Locate every malaria parasite and every leukocyte.
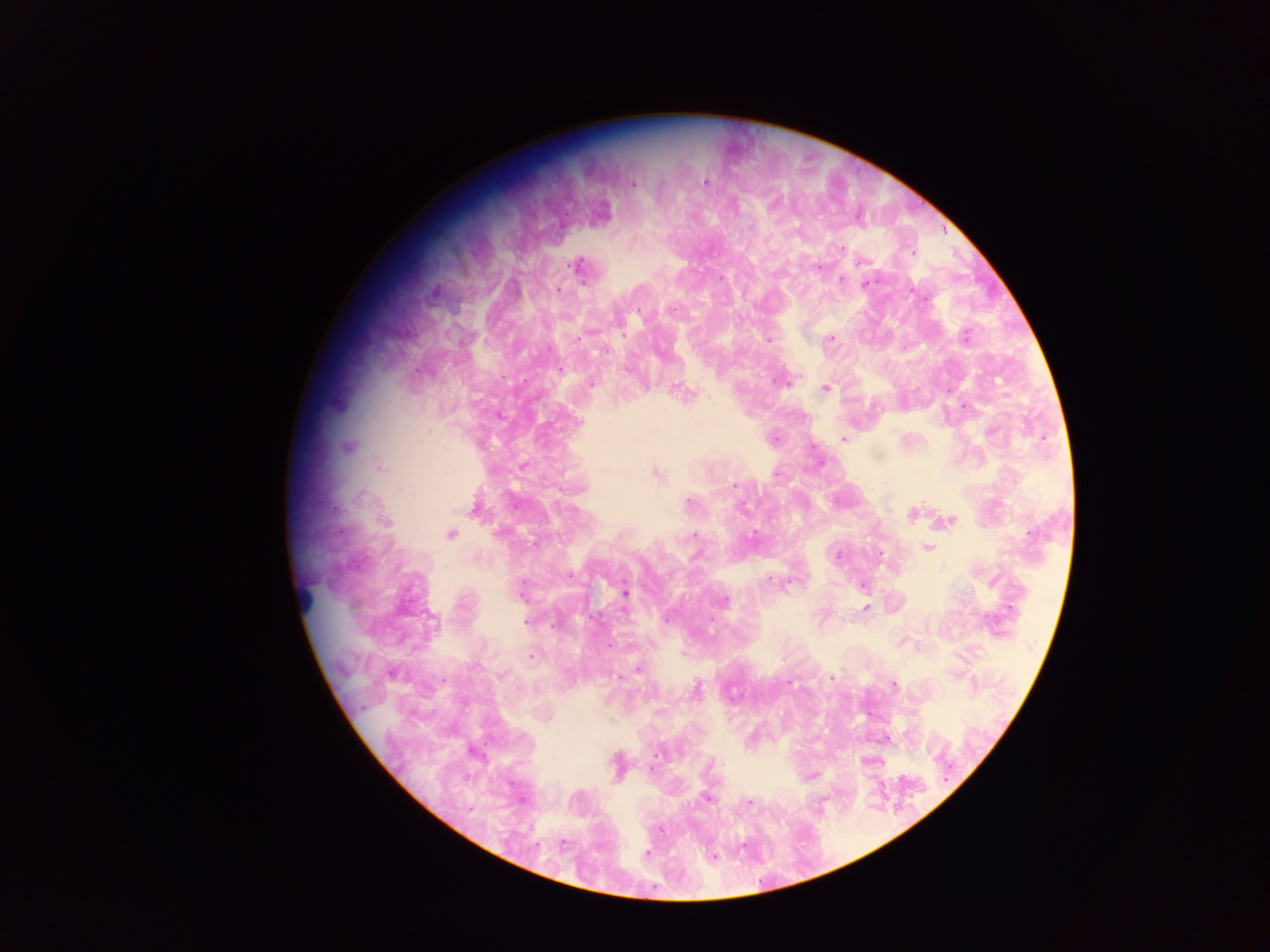

Approximate centers as [x, y] in pixels.
Malaria parasites: [705, 181], [632, 184], [842, 248], [912, 252], [862, 261], [577, 266], [819, 267], [721, 278], [841, 280], [866, 284], [558, 289], [638, 310], [670, 310], [965, 335], [579, 338], [830, 339], [768, 340], [605, 351], [559, 370], [778, 381], [591, 384], [824, 388], [965, 406], [843, 438], [774, 439], [346, 447], [380, 467], [657, 474], [734, 485], [689, 503], [912, 514], [949, 521], [386, 522], [451, 534], [692, 536], [752, 536], [927, 548], [880, 554], [838, 555], [570, 576], [770, 580], [863, 586], [625, 593], [724, 601], [866, 608], [667, 619], [527, 621], [530, 657], [637, 668], [504, 675], [832, 678], [789, 683], [893, 685], [696, 690], [657, 753], [722, 764], [812, 776], [706, 797], [748, 802], [470, 809], [661, 829], [564, 844], [646, 854], [712, 856].
Leukocytes: [303, 596].

One field of view. Photographed through a microscope with a mobile-phone camera. Thick blood film. Image is 1270×952 pixels. Sample from Ghana.